Give the position of every Plasmodium parasite visible.
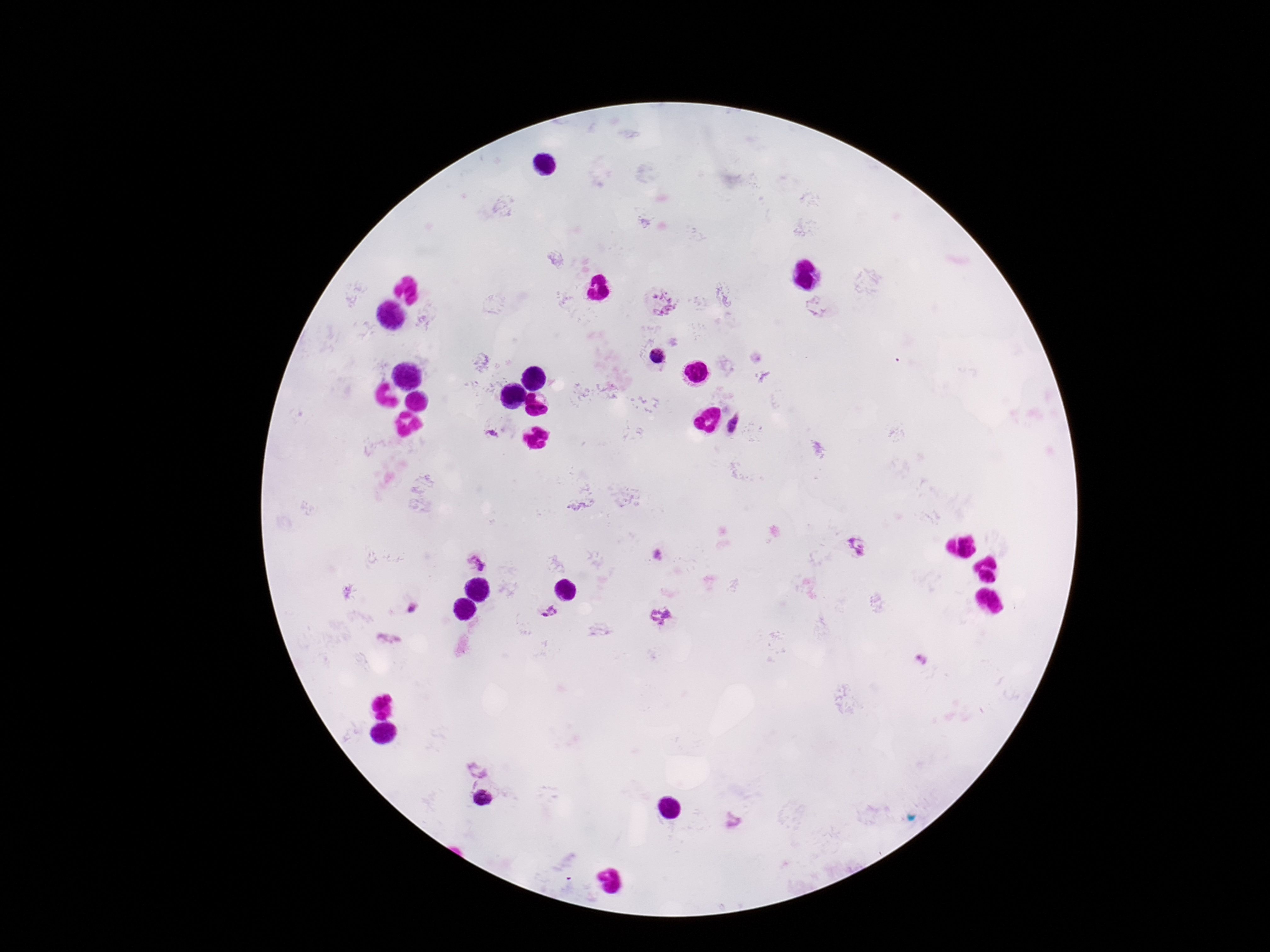

Approximate object centers, in pixels from the top-left corner.
Plasmodium parasites: (x=662, y=303), (x=657, y=355), (x=734, y=425), (x=491, y=434), (x=856, y=546), (x=477, y=561), (x=411, y=608), (x=549, y=611), (x=661, y=616), (x=480, y=770), (x=483, y=798).

Summary:
  - Image size: 1270×952 pixels
  - Field of view: single
  - Patient malaria status: positive
  - Magnification: 100x
  - Capture: smartphone camera through the microscope eyepiece
  - Stain: Giemsa
  - Preparation: thick blood smear